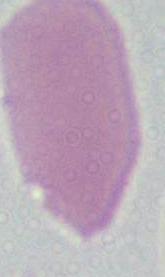 Micrograph. An erythrocyte is seen. Captured at 1000x magnification.